Assess this cell for malaria.
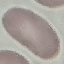
It is uninfected.

capture: smartphone through the microscope eyepiece
image_type: automatically extracted cell patch, resized to 64 × 64 pixels
preparation: thin blood smear
stain: Giemsa